Report the malaria status of this cell.
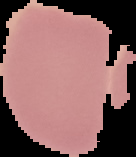

It is uninfected.

Summary:
  - Image type: cell region segmented out of the field of view; surrounding area masked to black
  - Image size: 136×157 pixels
  - Preparation: thin blood smear